Outline each blood parasite and name the species.
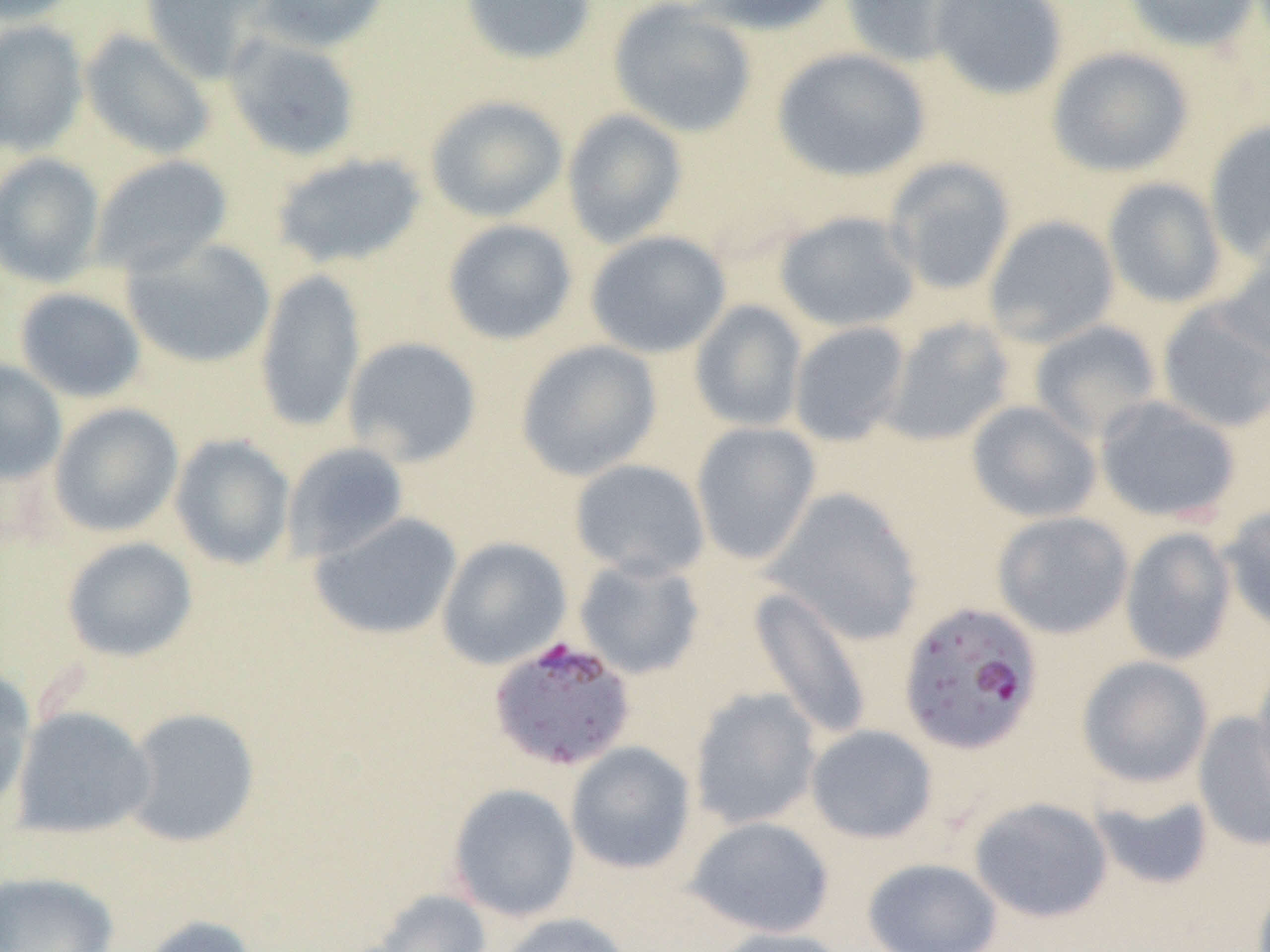

Approximate bounding boxes as [x1, y1, x2, y2] in pixels.
Plasmodium falciparum-infected red blood cells: [897, 600, 1044, 755], [488, 635, 638, 772].
No Plasmodium ovale, Plasmodium malariae, Plasmodium vivax, Babesia divergens, or Trypanosoma brucei observed.

Summary:
  - Uninfected red blood cell locations: [0, 0, 84, 26], [140, 0, 273, 83], [250, 0, 392, 54], [458, 0, 597, 66], [687, 0, 845, 36], [839, 0, 973, 69], [929, 0, 1069, 101], [1123, 0, 1262, 53], [607, 1, 758, 139], [0, 19, 88, 157], [80, 29, 215, 160], [222, 32, 362, 162], [1046, 46, 1194, 177], [772, 47, 932, 183], [425, 95, 568, 223], [562, 109, 688, 248], [1203, 121, 1270, 260], [0, 152, 105, 287], [271, 152, 427, 270], [88, 154, 234, 278], [883, 157, 1016, 296], [1102, 177, 1227, 309], [774, 210, 921, 333], [983, 215, 1120, 347], [441, 219, 578, 346], [585, 230, 732, 359], [1215, 236, 1270, 362], [122, 238, 276, 369], [255, 269, 367, 433], [14, 287, 147, 404], [689, 300, 808, 432], [1156, 301, 1270, 434], [882, 317, 1015, 447], [1029, 320, 1162, 443], [788, 321, 910, 447], [342, 336, 484, 468], [515, 339, 663, 481], [0, 358, 67, 485], [1094, 396, 1241, 524], [966, 400, 1102, 523], [48, 403, 184, 538], [690, 421, 822, 565], [170, 434, 295, 570], [281, 441, 409, 563], [569, 458, 710, 580], [764, 487, 925, 645], [1221, 505, 1270, 634], [310, 511, 462, 641], [992, 511, 1134, 639], [1119, 527, 1236, 665], [437, 536, 572, 670], [61, 537, 198, 663], [573, 557, 706, 679], [747, 586, 873, 742], [1076, 655, 1214, 789], [1252, 655, 1270, 805], [0, 667, 36, 816], [689, 687, 822, 830], [11, 706, 155, 840], [122, 707, 261, 848], [1194, 711, 1270, 852], [805, 724, 938, 844], [565, 741, 696, 875], [447, 783, 580, 922], [1089, 784, 1215, 890], [969, 796, 1113, 922], [685, 815, 835, 938], [862, 857, 1003, 952], [0, 870, 119, 952], [370, 888, 491, 952], [498, 912, 634, 952], [135, 914, 261, 952], [709, 926, 853, 952]
  - Slide-level diagnosis: Plasmodium falciparum
  - Field of view: single
  - Image size: 1270×952 pixels
  - Preparation: thin blood smear
  - Magnification: 1000x
  - Modality: optical microscopy